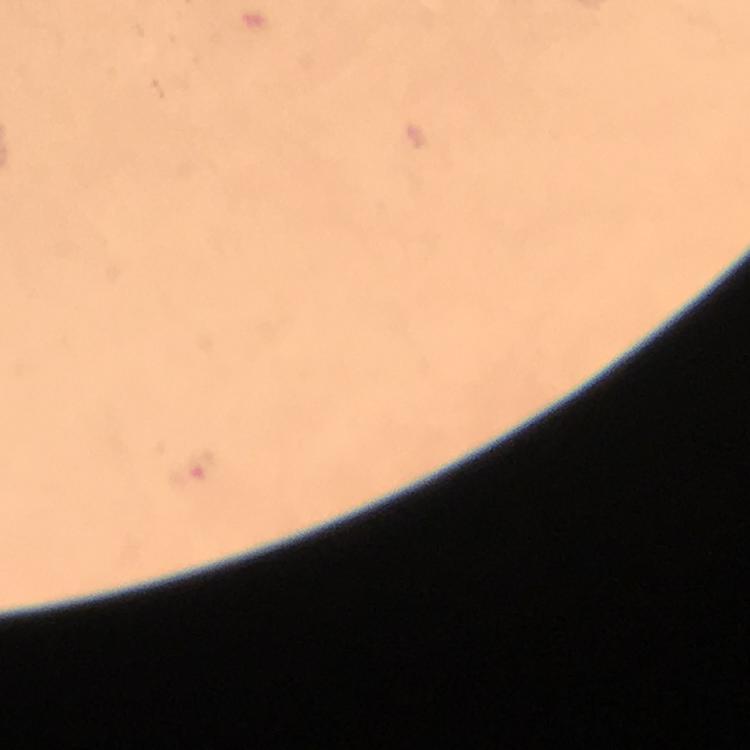

Approximate object centers, in pixels from the top-left corner. Malaria parasite locations: (x=194, y=470). Immersion oil applied. A crop from one field of view. 100x magnification. Giemsa-stained preparation. Smartphone photograph taken through a microscope. From a diagnostic examination for malaria. Thick blood smear. Image is 750×750 pixels.